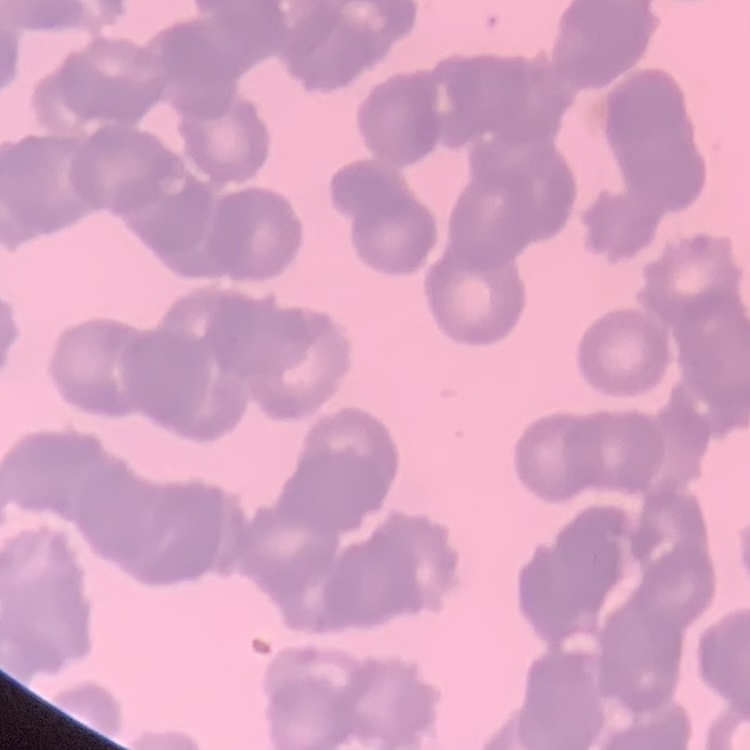

The erythrocytes show rouleaux formation. Thin peripheral smear. One tile cut from a larger photomicrograph. Stained with either Field's or Giemsa.